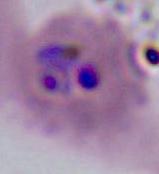

Summary:
  - Modality: photomicrograph
  - Magnification: 400x or 1000x
  - Identification: Plasmodium